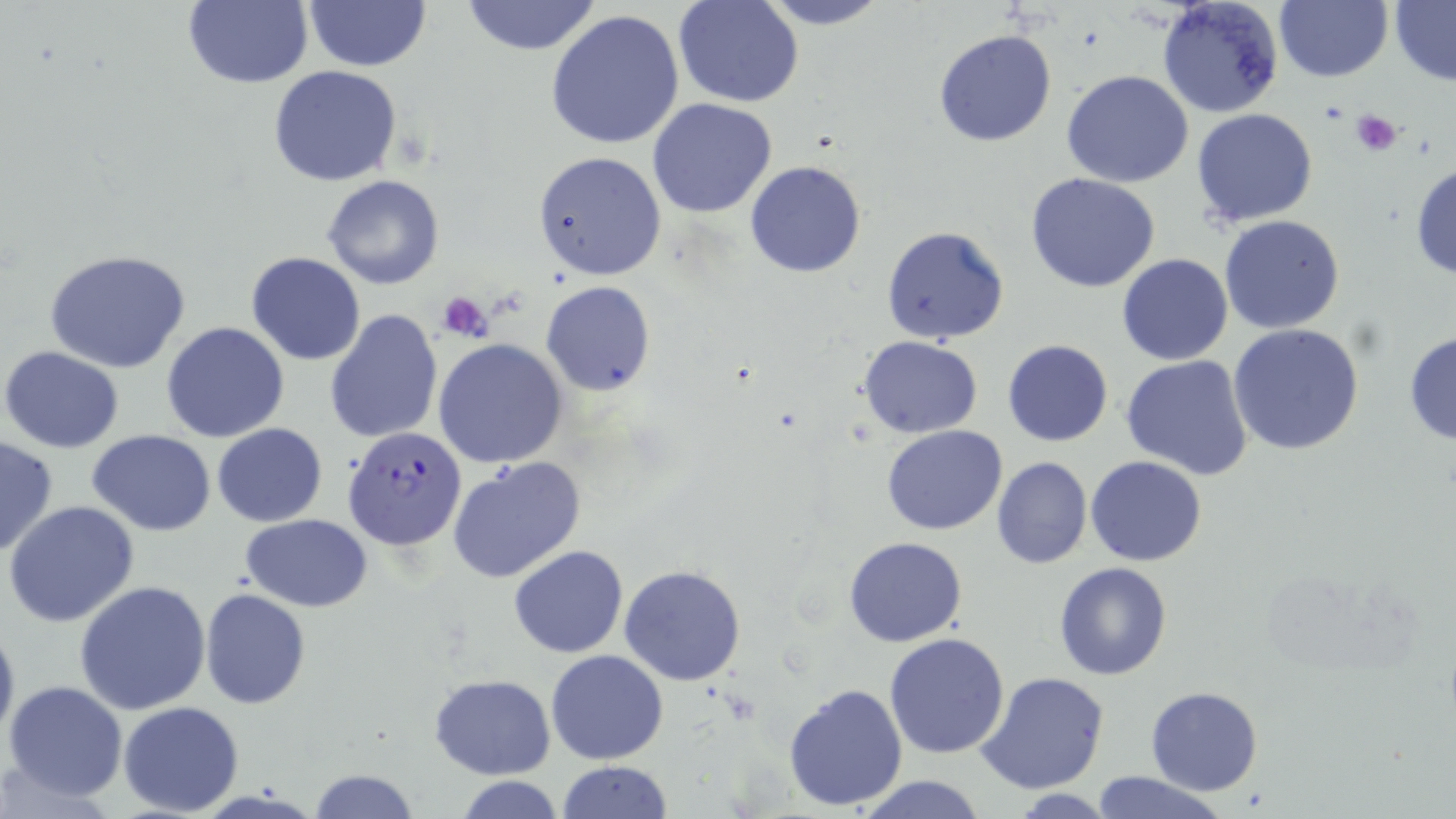
Summary:
  - Coordinate format: approximate bounding boxes as [x1, y1, x2, y2] in pixels
  - Uninfected red blood cell locations: [182, 0, 313, 89], [458, 0, 604, 55], [755, 0, 892, 30], [1158, 0, 1283, 118], [1273, 0, 1391, 83], [303, 1, 432, 71], [674, 1, 803, 107], [1389, 2, 1455, 83], [546, 10, 686, 150], [933, 28, 1057, 147], [268, 65, 405, 186], [1061, 71, 1194, 188], [647, 98, 778, 218], [1191, 108, 1318, 228], [533, 151, 668, 281], [1409, 160, 1456, 281], [745, 161, 867, 278], [1026, 172, 1162, 293], [321, 173, 444, 290], [1218, 214, 1346, 334], [879, 226, 1009, 345], [44, 249, 192, 373], [246, 252, 364, 365], [1117, 252, 1233, 366], [541, 281, 655, 395], [326, 309, 442, 443], [161, 322, 291, 442], [1229, 323, 1364, 455], [1404, 330, 1456, 446], [858, 337, 983, 437], [434, 339, 568, 468], [1002, 339, 1113, 446], [1, 346, 125, 454], [1122, 355, 1253, 480], [213, 423, 327, 526], [880, 424, 1006, 534], [89, 430, 216, 535], [0, 434, 59, 558], [446, 455, 587, 584], [1085, 456, 1208, 567], [992, 457, 1092, 570], [4, 501, 141, 628], [243, 515, 372, 610], [843, 536, 967, 647], [509, 545, 629, 658], [1053, 561, 1175, 680], [620, 563, 746, 685], [74, 581, 212, 715], [200, 589, 311, 708], [0, 614, 19, 752], [883, 632, 1011, 759], [546, 649, 669, 765], [975, 672, 1109, 795], [431, 674, 555, 779], [3, 680, 128, 803], [783, 683, 909, 813], [1145, 685, 1264, 795], [118, 701, 245, 816], [557, 761, 672, 817], [311, 767, 416, 819], [1085, 773, 1229, 819], [851, 774, 991, 818], [455, 777, 565, 817]
  - Plasmodium falciparum-infected red blood cell locations: [343, 427, 467, 552]
  - Platelet locations: [1349, 109, 1404, 157], [436, 292, 493, 342]
  - Slide-level diagnosis: Plasmodium falciparum
  - Image size: 1456×819 pixels
  - Preparation: thin blood film
  - Stain: May-Grünwald-Giemsa
  - Modality: optical microscopy
  - Magnification: 1000x
  - Field of view: single